Assess for Plasmodium parasites.
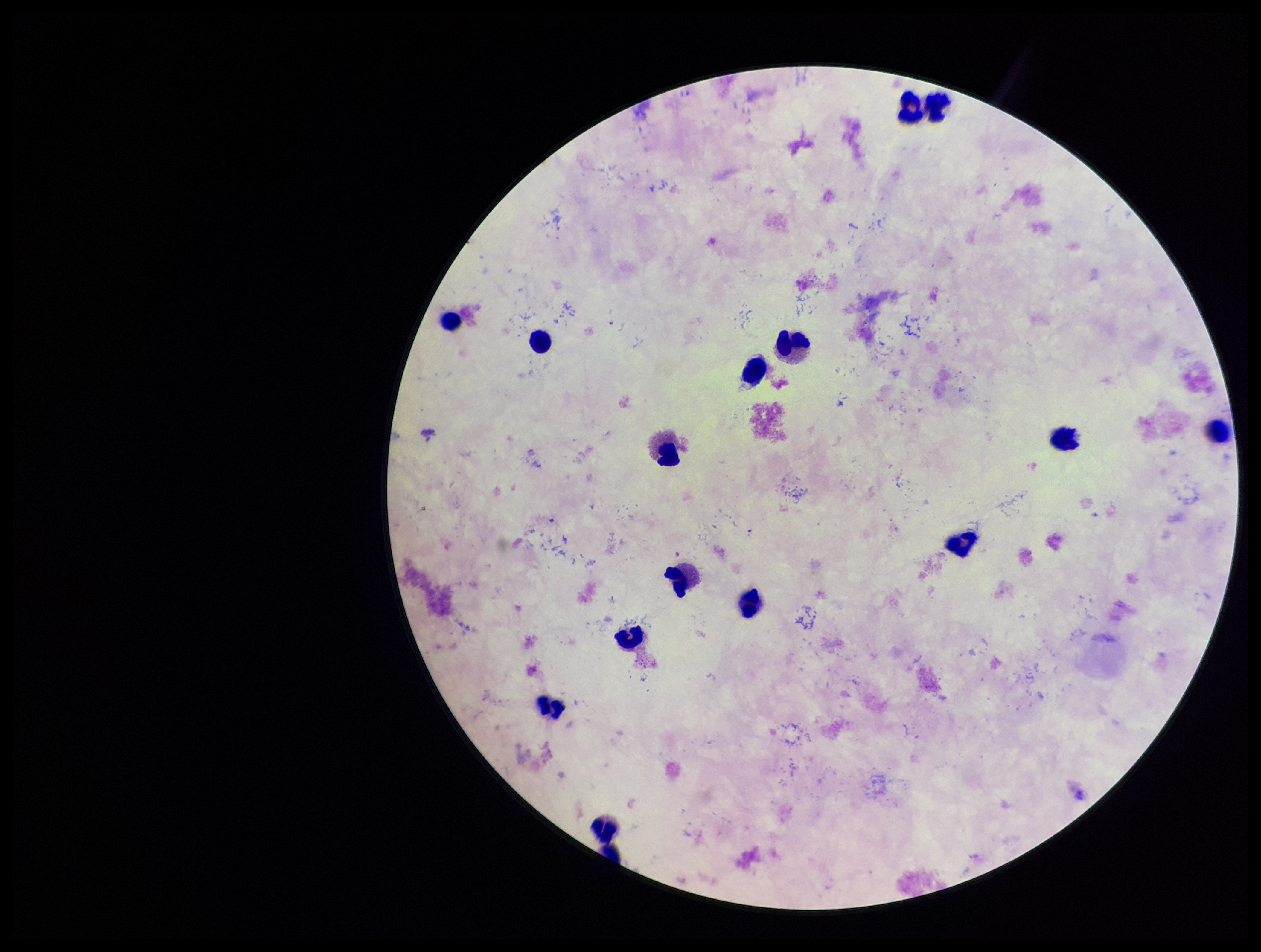
None identified.

preparation = thick blood smear
capture = smartphone photograph through the microscope eyepiece
species reported for this patient = Plasmodium falciparum
patient malaria status = positive
leukocyte count = 16
image size = 1261×952 pixels
stain = Giemsa
field of view = single
parasite count = 0